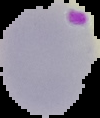
preparation = thin blood film
image type = cell region segmented out of the field of view; surrounding area masked to black
malaria status = parasitized
image size = 100×118 pixels